Outline each Plasmodium ovale-infected red blood cell.
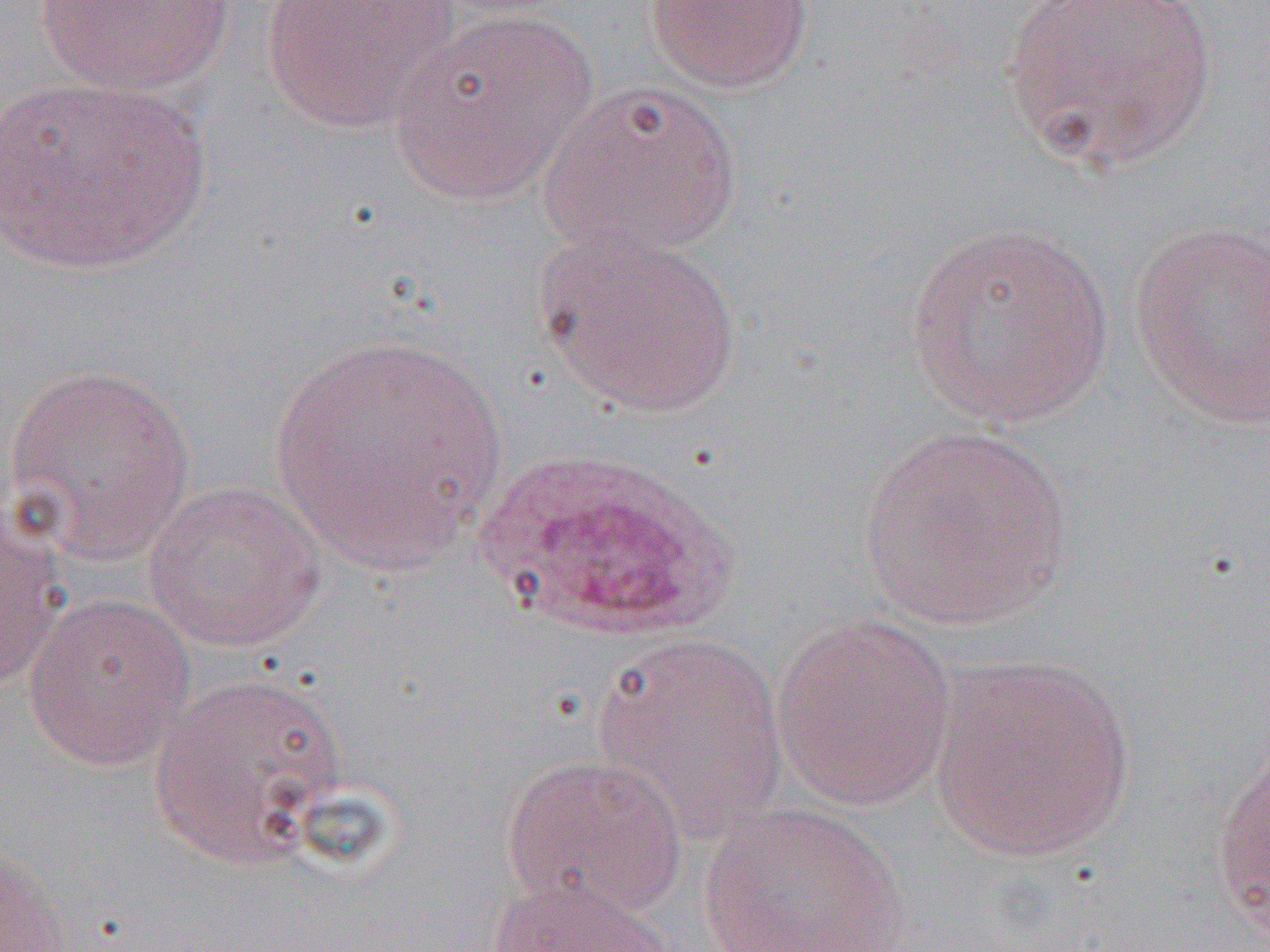

Approximate bounding boxes as named x1/y1/x2/y2 corners in pixels.
Plasmodium ovale-infected red blood cells: (x1=472, y1=446, x2=746, y2=644).

Uninfected red blood cell locations: (x1=261, y1=0, x2=460, y2=132), (x1=644, y1=0, x2=815, y2=93), (x1=1001, y1=0, x2=1221, y2=175), (x1=35, y1=1, x2=237, y2=95), (x1=388, y1=8, x2=597, y2=205), (x1=1, y1=76, x2=212, y2=276), (x1=539, y1=80, x2=744, y2=261), (x1=904, y1=221, x2=1116, y2=431), (x1=1128, y1=221, x2=1270, y2=431), (x1=537, y1=228, x2=742, y2=417), (x1=270, y1=333, x2=508, y2=572), (x1=4, y1=362, x2=198, y2=566), (x1=858, y1=424, x2=1074, y2=630), (x1=144, y1=480, x2=328, y2=652), (x1=0, y1=505, x2=69, y2=694), (x1=23, y1=593, x2=196, y2=770), (x1=770, y1=612, x2=958, y2=812), (x1=593, y1=633, x2=790, y2=844), (x1=928, y1=653, x2=1136, y2=863), (x1=148, y1=669, x2=350, y2=869), (x1=1210, y1=743, x2=1270, y2=942), (x1=500, y1=752, x2=687, y2=920), (x1=697, y1=802, x2=908, y2=952), (x1=0, y1=842, x2=76, y2=952), (x1=488, y1=871, x2=677, y2=952). Slide-level diagnosis: Plasmodium ovale. Image is 1270×952 pixels. Captured at 1000x magnification. Thin blood film. Single field of view. Optical microscopy.